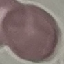
malaria status = uninfected
capture = smartphone through the microscope eyepiece
stain = Giemsa
preparation = thin blood film
image type = automatically extracted cell patch, resized to 64 × 64 pixels